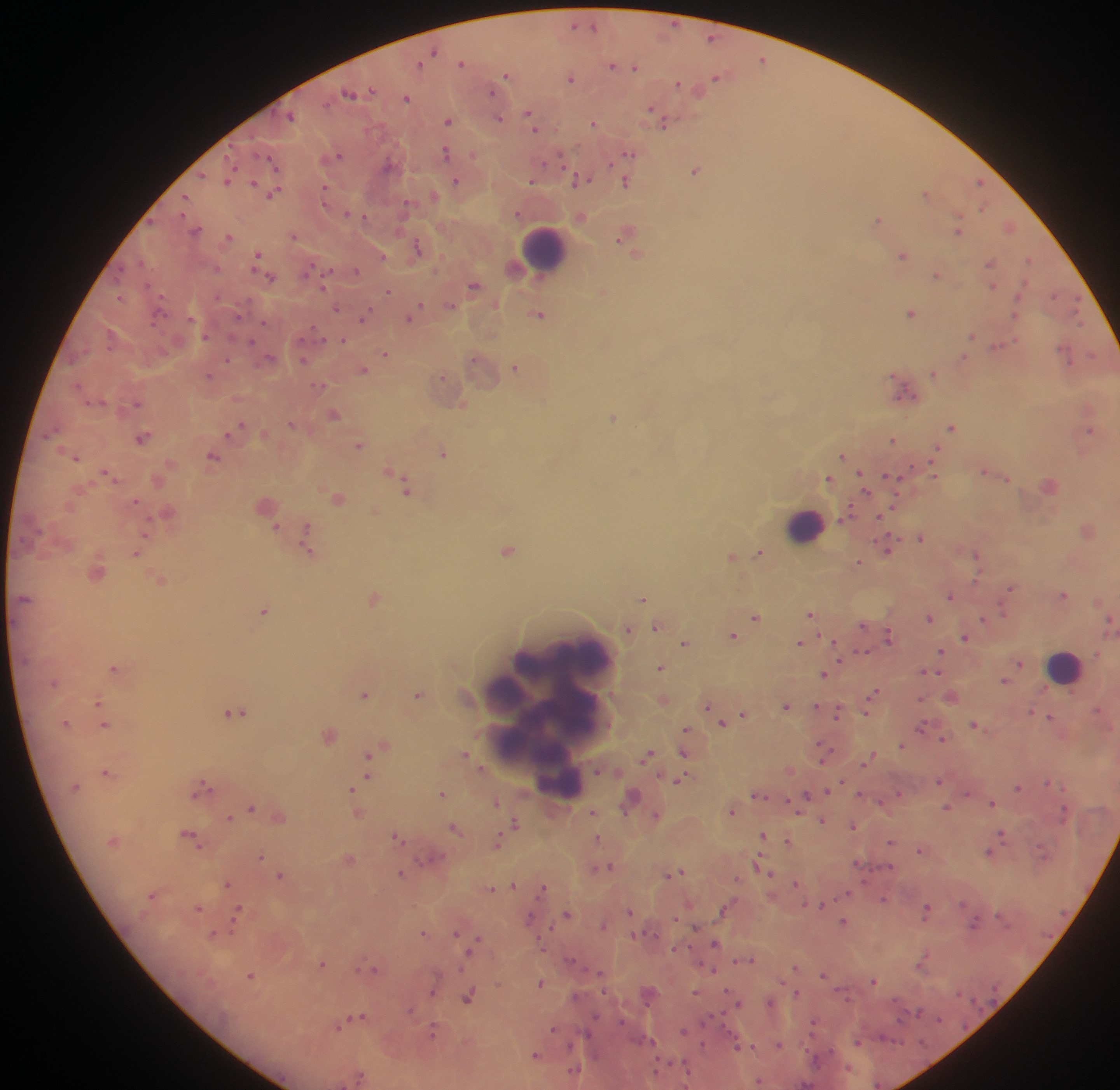
Approximate centers as x y in pixels. Plasmodium parasite locations: 574 23; 595 25; 711 37; 434 50; 762 58; 462 62; 419 64; 612 64; 636 66; 507 74; 715 75; 572 78; 678 83; 371 89; 491 91; 349 92; 406 97; 650 108; 529 112; 292 115; 498 117; 448 120; 594 122; 665 123; 534 128; 446 152; 628 153; 339 154; 560 158; 273 161; 387 164; 233 165; 696 170; 203 174; 228 178; 456 180; 532 180; 581 180; 254 181; 626 182; 978 182; 325 192; 925 192; 273 193; 185 197; 405 204; 982 207; 347 213; 518 213; 581 215; 365 216; 878 219; 1009 225; 957 229; 196 230; 623 233; 293 235; 230 236; 417 246; 258 254; 638 254; 383 255; 903 255; 1029 258; 142 261; 990 261; 217 268; 356 269; 936 274; 270 277; 325 282; 474 284; 991 285; 388 291; 602 291; 120 295; 419 305; 451 305; 337 307; 910 312; 1015 312; 538 313; 238 314; 1078 314; 363 317; 409 318; 264 321; 205 335; 972 335; 342 339; 253 341; 997 345; 385 352; 1064 352; 1092 354; 269 357; 963 357; 474 358; 227 359; 303 359; 516 367; 363 369; 933 373; 209 375; 441 376; 78 384; 320 385; 905 391; 136 403; 334 414; 613 416; 291 424; 951 426; 236 427; 54 429; 1089 429; 143 437; 894 439; 359 445; 443 451; 934 452; 842 455; 213 456; 76 457; 389 469; 985 470; 107 472; 934 473; 861 474; 892 477; 828 478; 1007 478; 406 487; 864 489; 338 498; 135 500; 848 513; 879 517; 275 527; 308 535; 921 536; 307 547; 888 547; 508 549; 137 552; 759 552; 976 553; 732 555; 859 560; 977 578; 161 579; 1010 588; 1063 594; 951 595; 24 597; 374 598; 642 598; 265 609; 1002 610; 811 613; 755 616; 929 617; 984 619; 1109 621; 862 624; 656 626; 628 629; 734 634; 888 636; 964 637; 684 643; 799 643; 941 650; 864 652; 840 661; 1020 662; 113 667; 660 667; 924 672; 937 672; 824 673; 1005 680; 874 692; 364 693; 418 693; 921 698; 98 701; 816 705; 707 706; 785 706; 1098 708; 1031 711; 234 712; 838 712; 866 712; 743 713; 1050 716; 722 723; 974 723; 105 725; 921 726; 686 729; 329 735; 944 739; 902 744; 381 746; 373 752; 684 752; 465 753; 647 754; 823 754; 873 755; 369 761; 106 771; 368 771; 678 779; 939 780; 842 781; 363 782; 1048 782; 203 785; 1017 787; 352 788; 829 789; 442 793; 807 793; 860 793; 967 793; 757 795; 632 797; 496 802; 992 802; 252 807; 945 807; 593 811; 733 811; 358 813; 657 815; 229 817; 822 819; 515 822; 853 825; 455 828; 1002 832; 762 834; 190 835; 396 837; 597 837; 788 840; 890 840; 497 843; 919 849; 1043 852; 989 853; 260 855; 350 858; 429 858; 757 863; 608 866; 890 866; 679 871; 400 872; 770 873; 280 875; 737 878; 796 883; 226 884; 512 884; 544 887; 490 888; 847 893; 153 894; 884 898; 963 903; 822 906; 198 907; 926 909; 237 912; 630 912; 567 914; 529 916; 1000 916; 844 921; 973 924; 603 925; 234 926; 695 926; 423 933; 456 933; 214 934; 633 935; 476 942; 715 942; 675 948; 751 959; 923 959; 570 960; 322 963; 463 966; 796 968; 375 969; 714 969; 250 975; 824 975; 873 980; 541 982; 433 988; 695 992; 797 993; 468 997; 770 1002; 739 1003; 410 1010; 919 1011; 361 1016; 939 1018; 621 1021; 813 1023; 338 1025; 552 1028; 432 1030; 683 1031; 651 1040; 858 1041; 778 1044; 738 1046; 753 1046; 535 1054; 574 1071; 758 1081. Leukocyte locations: 546 246; 805 523; 567 662; 1065 664; 502 692; 513 699; 550 718; 560 780. Mobile-phone photograph taken through the microscope. Image is 1120×1090 pixels. Single field of view. Collected in Ghana. Thick blood smear.